Give the position of every Plasmodium parasite.
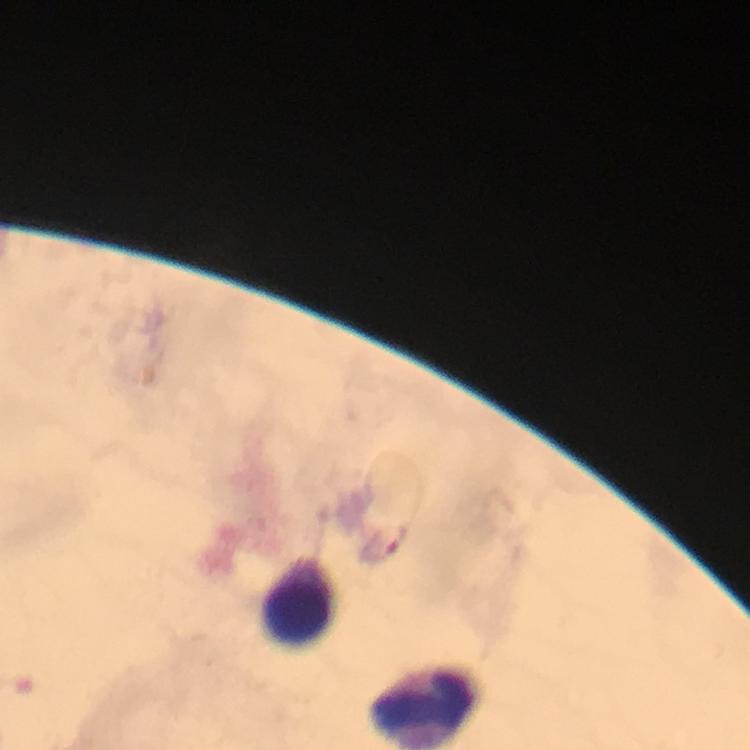
No Plasmodium parasites seen.

magnification = 100x
cropped from = a single field of view
immersion oil = used
image size = 750×750 pixels
stain = Giemsa
capture = smartphone mounted on the microscope
preparation = thick smear
context = from a malaria diagnostic workup
leukocyte locations = approximate centers as {x, y} in pixels: {301, 599}, {425, 705}